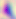
Summary:
  - Modality: micrograph
  - Identification: Toxoplasma gondii
  - Magnification: 400x